Classify this cell by malaria status.
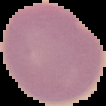
It is uninfected.

preparation: thin blood film
image_type: segmented cell region on a black background
image_size: 106×106 pixels